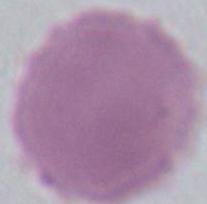

magnification = 1000x
modality = photomicrograph
identification = red blood cell